Classify this cell by malaria status.
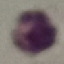
Uninfected.

Thin blood smear. Photographed with a smartphone camera at the microscope eyepiece. Automatically extracted cell patch, resized to 64 × 64 pixels. Giemsa stain.